Identify the preparation type.
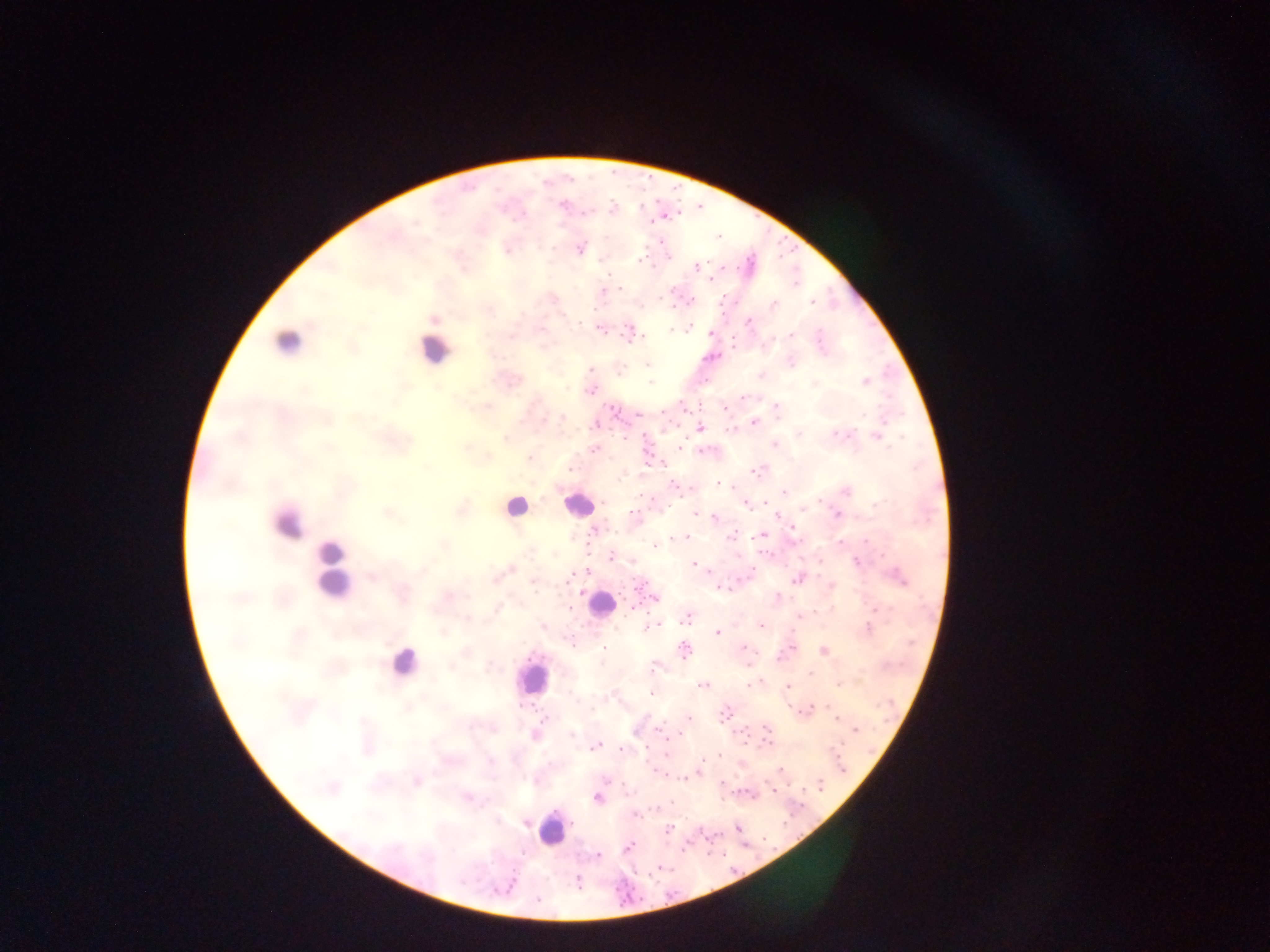
Thick blood film.

Approximate centers as x y in pixels. Plasmodium parasite locations: 556 203; 561 206; 612 208; 516 219; 580 248; 506 250; 638 260; 695 267; 606 276; 711 277; 621 287; 603 295; 550 299; 663 300; 810 303; 773 305; 433 319; 750 321; 540 327; 599 328; 689 328; 668 330; 788 334; 509 335; 819 336; 632 337; 638 338; 735 344; 493 354; 791 359; 647 364; 593 369; 760 375; 864 380; 650 382; 814 382; 590 389; 304 390; 744 396; 486 408; 726 410; 561 416; 754 422; 700 428; 730 430; 835 432; 798 433; 847 433; 878 436; 623 437; 504 438; 775 445; 465 447; 678 447; 591 448; 486 457; 528 458; 570 470; 755 470; 750 471; 623 475; 719 480; 393 486; 674 486; 784 492; 846 492; 877 504; 460 508; 803 511; 385 513; 694 513; 836 516; 714 517; 778 517; 592 530; 791 533; 730 535; 673 537; 679 537; 684 537; 763 537; 868 541; 655 544; 443 545; 527 553; 612 557; 858 563; 691 564; 509 569; 896 574; 371 577; 568 577; 494 579; 796 580; 532 584; 831 585; 722 587; 580 591; 447 596; 653 597; 778 598; 632 606; 879 606; 497 608; 468 617; 799 617; 687 618; 543 625; 647 625; 653 625; 760 625; 867 626; 717 631; 443 632; 744 647; 684 650; 823 652; 779 657; 748 661; 451 666; 489 667; 656 667; 808 673; 748 684; 838 685; 704 687; 786 688; 652 693; 723 711; 804 711; 834 718; 687 719; 855 729; 661 731; 571 734; 667 735; 535 736; 767 743; 595 745; 623 749; 664 754; 717 756; 654 769; 780 769; 698 771; 660 773; 684 778; 608 781; 416 783; 772 790; 750 794; 468 797; 598 799; 636 815; 497 821; 526 823; 669 828; 736 829; 628 847; 597 855; 576 881; 537 898. Mobile-phone photograph taken through the microscope. Sample from Ghana. Single field of view. Image is 1270×952 pixels.